Locate every blood parasite and identify its species.
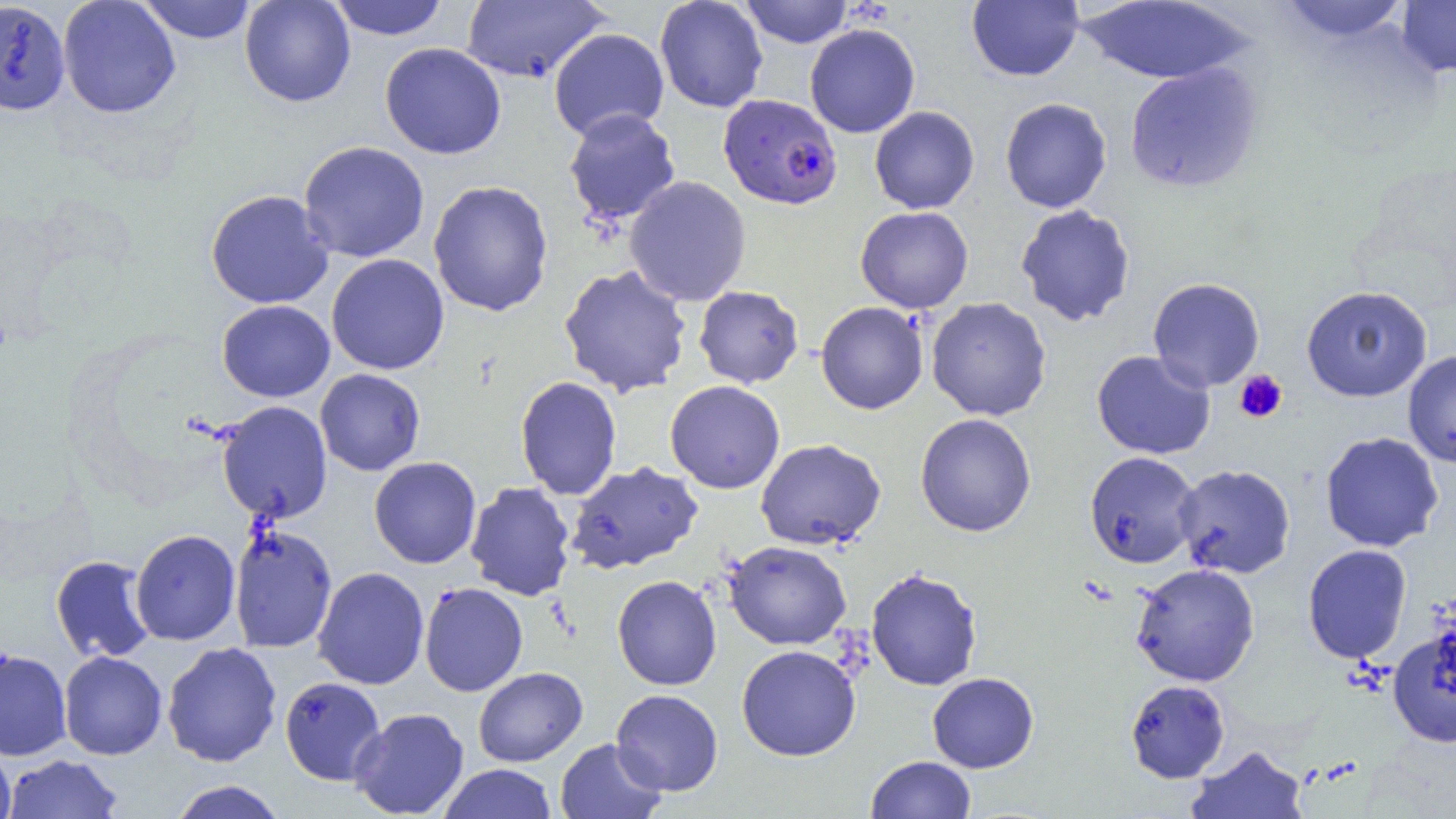
Approximate bounding boxes as (x1, y1, x2, y2) in pixels.
Plasmodium falciparum-infected red blood cells: (718, 94, 843, 210).
No Plasmodium ovale, Plasmodium malariae, Plasmodium vivax, Babesia divergens, or Trypanosoma brucei observed.

Uninfected red blood cell locations: (137, 0, 258, 44), (239, 0, 356, 107), (328, 0, 448, 40), (651, 0, 764, 113), (740, 0, 854, 48), (1275, 0, 1413, 45), (58, 1, 181, 118), (461, 1, 610, 83), (966, 1, 1084, 81), (1075, 1, 1254, 85), (1396, 1, 1456, 78), (0, 2, 70, 115), (804, 23, 920, 138), (548, 28, 669, 142), (379, 42, 506, 159), (1124, 61, 1263, 194), (1000, 97, 1112, 213), (869, 106, 979, 214), (563, 108, 681, 225), (298, 140, 430, 263), (624, 175, 751, 307), (428, 180, 554, 317), (205, 189, 334, 309), (1015, 204, 1136, 327), (855, 206, 974, 313), (326, 254, 450, 375), (558, 264, 692, 398), (1147, 277, 1265, 392), (694, 285, 804, 388), (1301, 285, 1433, 402), (926, 296, 1052, 421), (217, 300, 335, 402), (816, 301, 928, 414), (1092, 350, 1216, 459), (1403, 350, 1456, 468), (314, 368, 425, 476), (515, 376, 622, 501), (665, 380, 785, 494), (217, 401, 332, 523), (915, 413, 1036, 537), (1320, 431, 1444, 552), (755, 438, 886, 550), (1084, 451, 1201, 568), (369, 456, 481, 568), (566, 461, 703, 574), (1174, 464, 1295, 579), (465, 481, 576, 601), (229, 523, 338, 653), (130, 529, 240, 646), (724, 541, 852, 650), (1302, 544, 1412, 664), (50, 555, 156, 663), (1131, 563, 1260, 687), (313, 566, 429, 690), (865, 568, 983, 691), (612, 575, 721, 690), (419, 582, 528, 696), (1387, 627, 1456, 748), (162, 642, 282, 767), (736, 645, 861, 761), (0, 648, 71, 761), (59, 651, 167, 760), (473, 667, 588, 766), (927, 672, 1039, 773), (280, 677, 386, 785), (1125, 679, 1230, 783), (611, 689, 723, 796), (349, 707, 469, 818), (555, 738, 667, 819), (0, 744, 16, 819), (1187, 745, 1308, 819), (3, 754, 125, 819), (866, 755, 976, 818), (438, 763, 557, 819), (167, 780, 288, 819). Platelet locations: (1234, 369, 1288, 424). Slide-level diagnosis: Plasmodium falciparum. Captured at 1000x magnification. Image is 1456×819 pixels. Single field of view. Light microscopy. Thin blood film.